Classify this cell by malaria status.
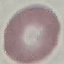
Uninfected.

Summary:
  - Capture: smartphone camera at the microscope eyepiece
  - Preparation: thin blood smear
  - Image type: automatically extracted cell patch, resized to 64 × 64 pixels
  - Stain: Giemsa